Identify the blood parasite species.
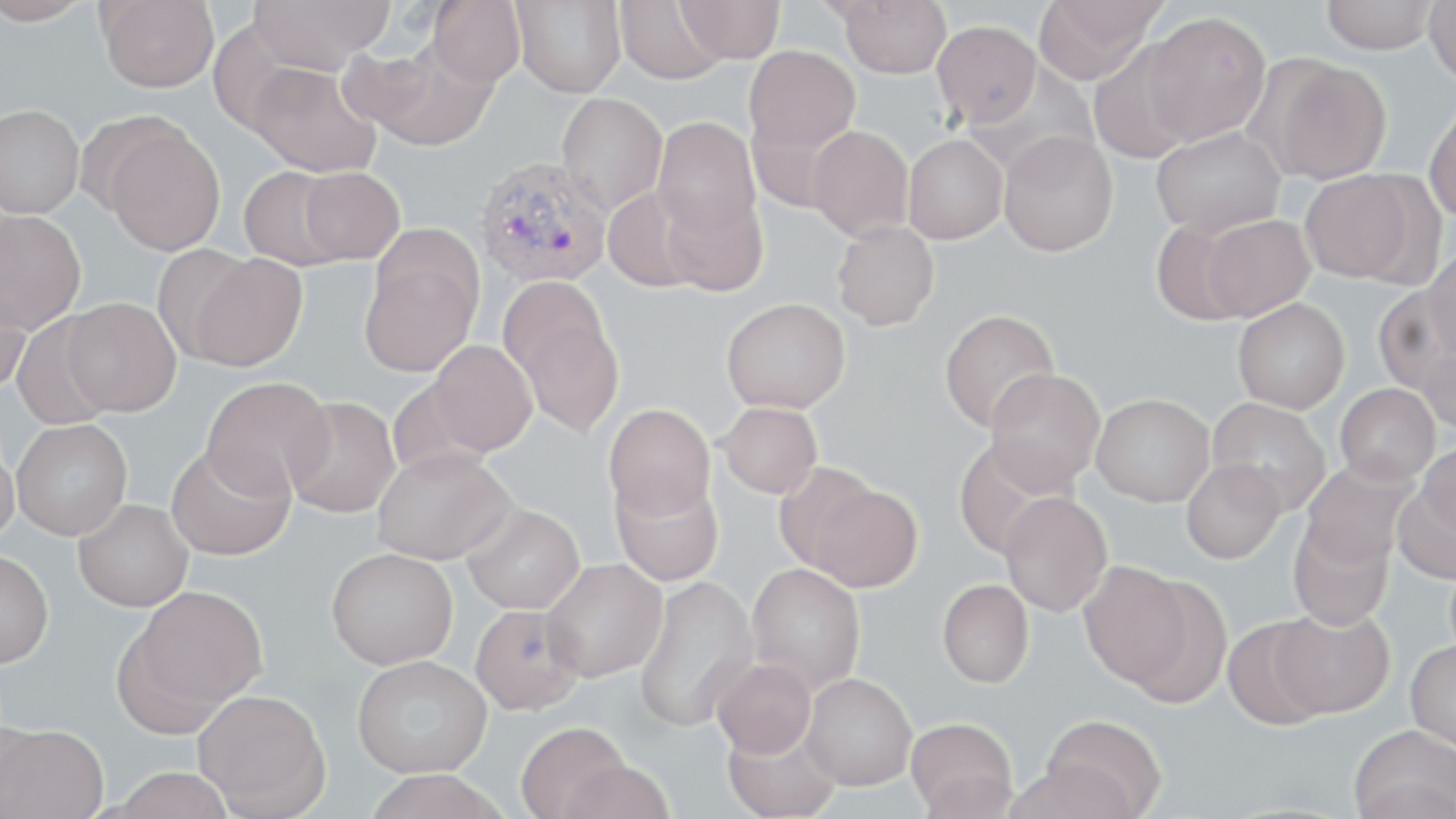

Plasmodium vivax.

{
  "uninfected_red_blood_cell_locations": "approximate bounding boxes as (x1, y1, x2, y2) in pixels: (0, 0, 94, 26), (98, 0, 219, 93), (247, 0, 395, 72), (513, 0, 626, 98), (613, 0, 729, 84), (1034, 0, 1164, 83), (1322, 0, 1438, 54), (1423, 0, 1456, 86), (428, 1, 526, 87), (675, 1, 785, 64), (837, 1, 952, 78), (1140, 11, 1272, 145), (932, 20, 1041, 127), (358, 41, 496, 150), (1088, 43, 1197, 164), (744, 45, 860, 155), (1261, 58, 1392, 183), (246, 60, 382, 178), (555, 93, 667, 214), (1423, 99, 1456, 224), (0, 105, 84, 218), (653, 116, 760, 239), (102, 123, 225, 255), (807, 125, 914, 241), (1150, 126, 1285, 238), (998, 131, 1118, 257), (903, 134, 1008, 244), (238, 166, 350, 270), (299, 167, 405, 264), (1301, 170, 1418, 283), (603, 187, 703, 293), (660, 188, 768, 296), (0, 210, 86, 333), (1200, 214, 1315, 321), (1150, 220, 1252, 326), (832, 221, 939, 330), (152, 242, 261, 367), (1424, 250, 1456, 364), (187, 253, 308, 371), (360, 256, 479, 377), (497, 276, 611, 381), (0, 280, 32, 395), (1374, 288, 1452, 396), (721, 297, 851, 413), (61, 298, 181, 416), (1233, 298, 1349, 413), (938, 309, 1060, 433), (514, 310, 624, 438), (11, 314, 118, 430), (1416, 339, 1456, 436), (428, 340, 537, 455), (984, 368, 1106, 492), (202, 376, 334, 498), (385, 378, 492, 480), (1335, 383, 1440, 485), (1091, 394, 1215, 507), (284, 396, 400, 518), (1207, 397, 1331, 516), (718, 402, 822, 499), (604, 403, 715, 519), (11, 418, 133, 539), (953, 436, 1068, 560), (0, 441, 19, 544), (1418, 441, 1456, 541), (166, 442, 295, 560), (372, 447, 514, 564), (1181, 458, 1286, 564), (1299, 459, 1419, 568), (774, 461, 882, 573), (610, 473, 724, 586), (1393, 481, 1456, 585), (806, 483, 923, 592), (998, 492, 1113, 617), (74, 499, 193, 611), (462, 504, 585, 614), (1287, 517, 1395, 630), (326, 547, 458, 669), (0, 550, 54, 667), (541, 558, 667, 681), (1079, 560, 1195, 688), (747, 562, 866, 694), (633, 575, 759, 733), (1123, 576, 1233, 709), (937, 580, 1034, 687), (122, 585, 269, 720), (469, 604, 584, 715), (1268, 606, 1394, 719), (1221, 618, 1332, 729), (1406, 639, 1456, 752), (352, 655, 492, 779), (711, 657, 817, 759), (801, 673, 917, 789), (193, 689, 330, 816), (1040, 714, 1167, 818), (906, 717, 1018, 817), (1, 723, 109, 819), (515, 723, 632, 818), (722, 724, 841, 819), (1348, 725, 1456, 819), (557, 759, 676, 819), (109, 767, 238, 819), (363, 771, 510, 819)",
  "plasmodium_vivax_infected_red_blood_cell_locations": "approximate bounding boxes as (x1, y1, x2, y2) in pixels: (475, 156, 613, 287)",
  "image_size": "1456×819 pixels",
  "preparation": "thin blood film",
  "modality": "light microscopy",
  "stain": "May-Grünwald-Giemsa",
  "field_of_view": "single",
  "magnification": "1000x"
}